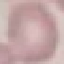
Malaria status: uninfected. Thin smear of blood. Giemsa-stained preparation. Acquired by smartphone through the microscope eyepiece. Cell patch, automatically extracted from a larger field of view and resized to 64 × 64 pixels.